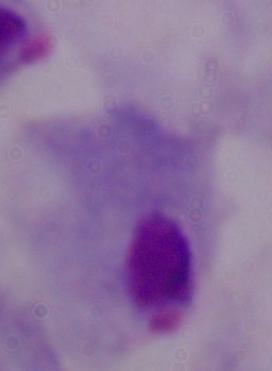

Summary:
  - Magnification: 1000x
  - Identification: trichomonad
  - Modality: micrograph